Assess this cell for malaria.
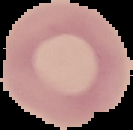
Uninfected.

From a thin blood smear. The area outside the segmented cell region is set to black. Image is 133×130 pixels.